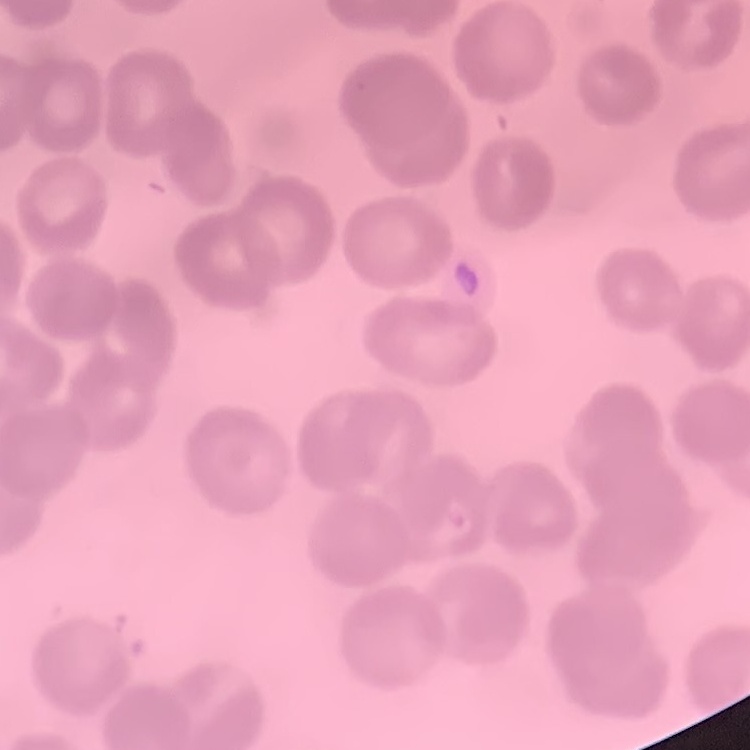

The erythrocytes show no rouleaux formation. Field's or Giemsa stain. Square crop of a larger photomicrograph. Thin blood film.